Identify the cell.
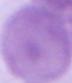
An erythrocyte.

Summary:
  - Magnification: 1000x
  - Modality: photomicrograph